State which parasite is depicted.
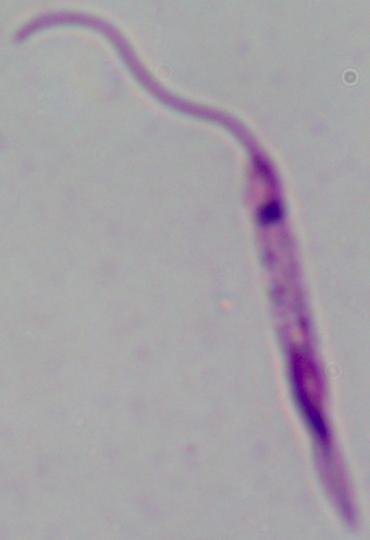

Leishmania.

1000x magnification. Micrograph.